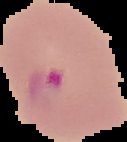
From a thin blood smear. Segmented cell region on a black background. Image is 127×142 pixels. Malaria status: parasitized.